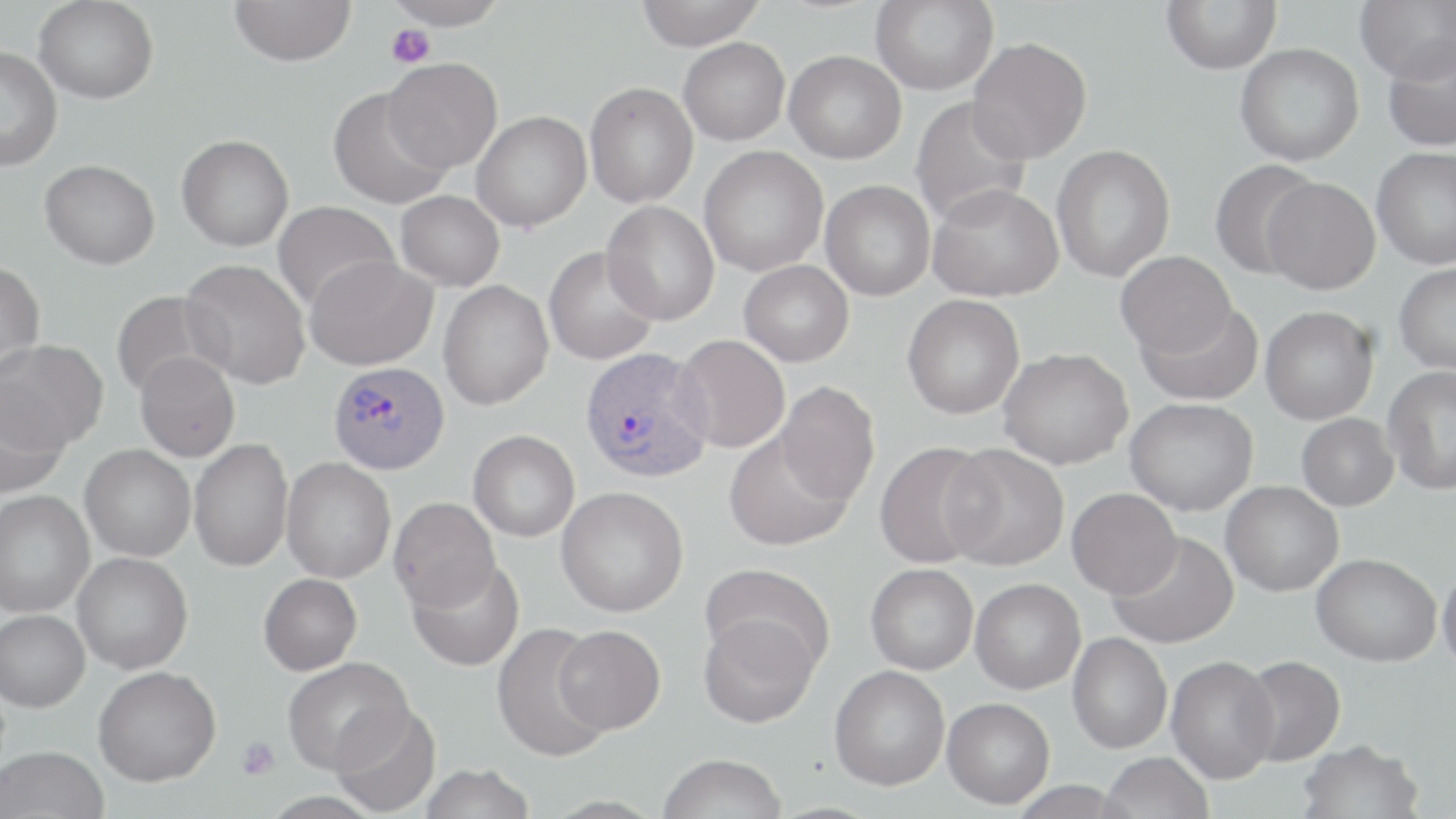 Approximate bounding boxes as (x1,y1)-(x2,y2) corner pairs in pixels. Uninfected red blood cell locations: (34,0)-(159,104), (229,0)-(356,67), (382,0)-(510,29), (634,0)-(766,50), (871,0)-(998,95), (1160,0)-(1282,74), (1354,0)-(1456,83), (1381,36)-(1456,152), (678,37)-(790,145), (967,37)-(1092,163), (1235,43)-(1364,166), (0,46)-(61,171), (784,51)-(907,164), (382,58)-(502,172), (584,82)-(698,208), (327,87)-(452,209), (909,96)-(1032,227), (471,111)-(592,232), (177,134)-(294,251), (1051,144)-(1175,282), (698,145)-(829,277), (1371,147)-(1456,269), (40,159)-(160,269), (1209,159)-(1321,280), (1262,177)-(1380,294), (820,180)-(935,301), (927,183)-(1064,302), (395,190)-(504,291), (272,201)-(399,313), (601,201)-(719,326), (543,246)-(659,365), (1115,251)-(1236,358), (304,255)-(437,371), (181,258)-(311,389), (739,259)-(854,366), (0,261)-(45,376), (1394,262)-(1456,375), (438,280)-(553,410), (112,291)-(224,399), (902,294)-(1025,419), (1137,301)-(1262,406), (1260,306)-(1379,424), (674,335)-(790,453), (1,339)-(108,451), (999,348)-(1134,469), (135,351)-(240,462), (1383,365)-(1456,496), (775,381)-(879,505), (0,385)-(70,497), (1125,397)-(1259,515), (1296,413)-(1399,511), (468,429)-(580,542), (724,431)-(853,551), (189,438)-(293,572), (874,441)-(996,568), (942,443)-(1069,570), (80,445)-(195,561), (281,456)-(396,583), (1220,481)-(1343,596), (556,486)-(688,616), (1067,488)-(1181,598), (0,491)-(94,617), (389,498)-(500,613), (1109,531)-(1240,649), (72,552)-(193,673), (1311,553)-(1441,666), (407,557)-(525,671), (1437,562)-(1456,675), (700,563)-(835,672), (866,563)-(979,674), (259,573)-(362,675), (970,579)-(1085,694), (0,609)-(90,712), (698,612)-(820,728), (491,622)-(611,763), (555,625)-(666,734), (1068,632)-(1172,753), (1237,655)-(1346,767), (1166,656)-(1280,783), (282,657)-(413,774), (829,665)-(950,790), (93,666)-(221,787), (942,697)-(1055,809), (330,703)-(441,817), (1297,738)-(1423,819), (0,746)-(110,819), (1100,751)-(1214,819), (657,754)-(787,819), (418,764)-(536,819). Platelet locations: (386,24)-(435,68), (237,737)-(279,780). Plasmodium vivax-infected red blood cell locations: (579,347)-(714,483), (328,361)-(449,475). Slide-level diagnosis: Plasmodium vivax. 1000x magnification. One field of a larger specimen. Light microscopy. May-Grünwald-Giemsa stain. Image is 1456×819 pixels. Thin blood smear.